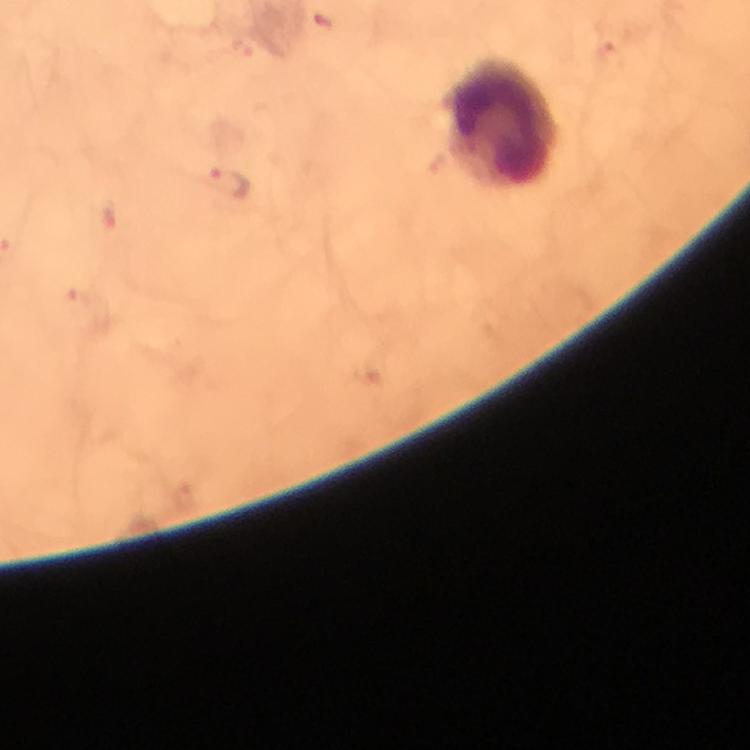
Approximate object centers, in pixels from the top-left corner. Leukocyte locations: (x=503, y=122). Malaria parasite locations: (x=230, y=181). Immersion oil was used. Cropped region of a single field of view. 100x magnification. Giemsa-stained preparation. Thick smear. From a diagnostic examination for malaria. Image is 750×750 pixels. Photographed with a smartphone mounted on the microscope.